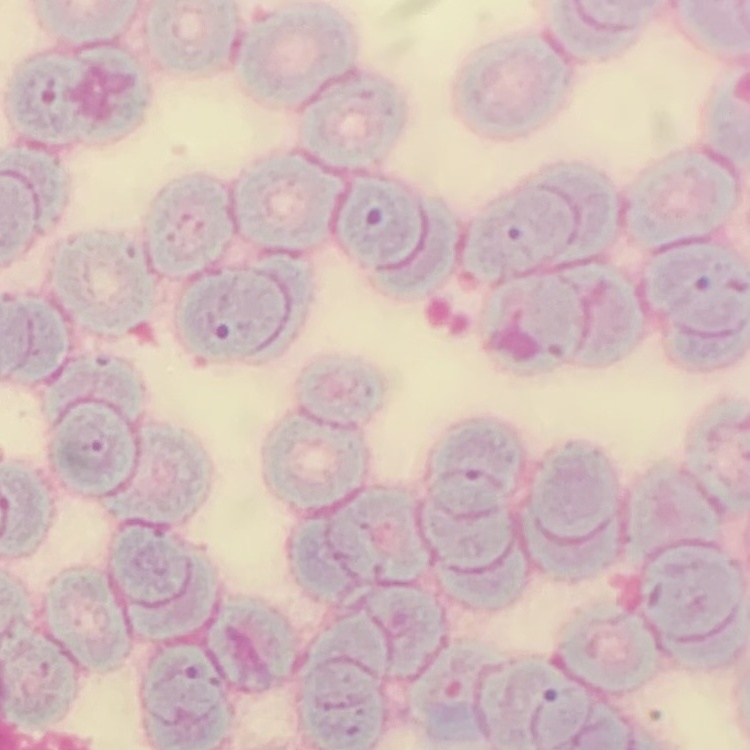
Summary:
  - Red blood cell morphology: rouleaux formation
  - Stain: Field's or Giemsa
  - Image type: square crop of a larger photomicrograph
  - Preparation: thin blood smear